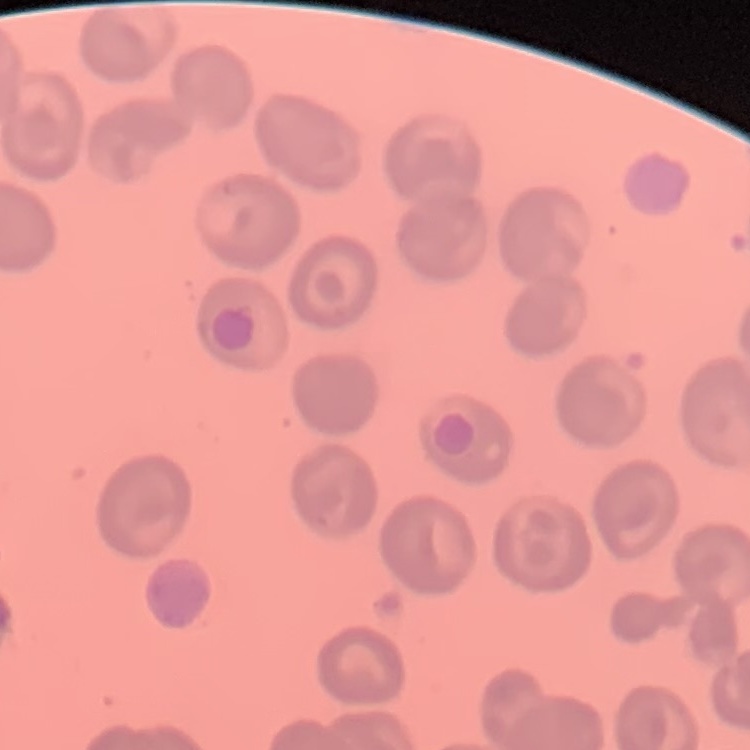 The erythrocytes exhibit no rouleaux formation. One tile cut from a larger photomicrograph. Thin blood film. Stained with either Field's or Giemsa.